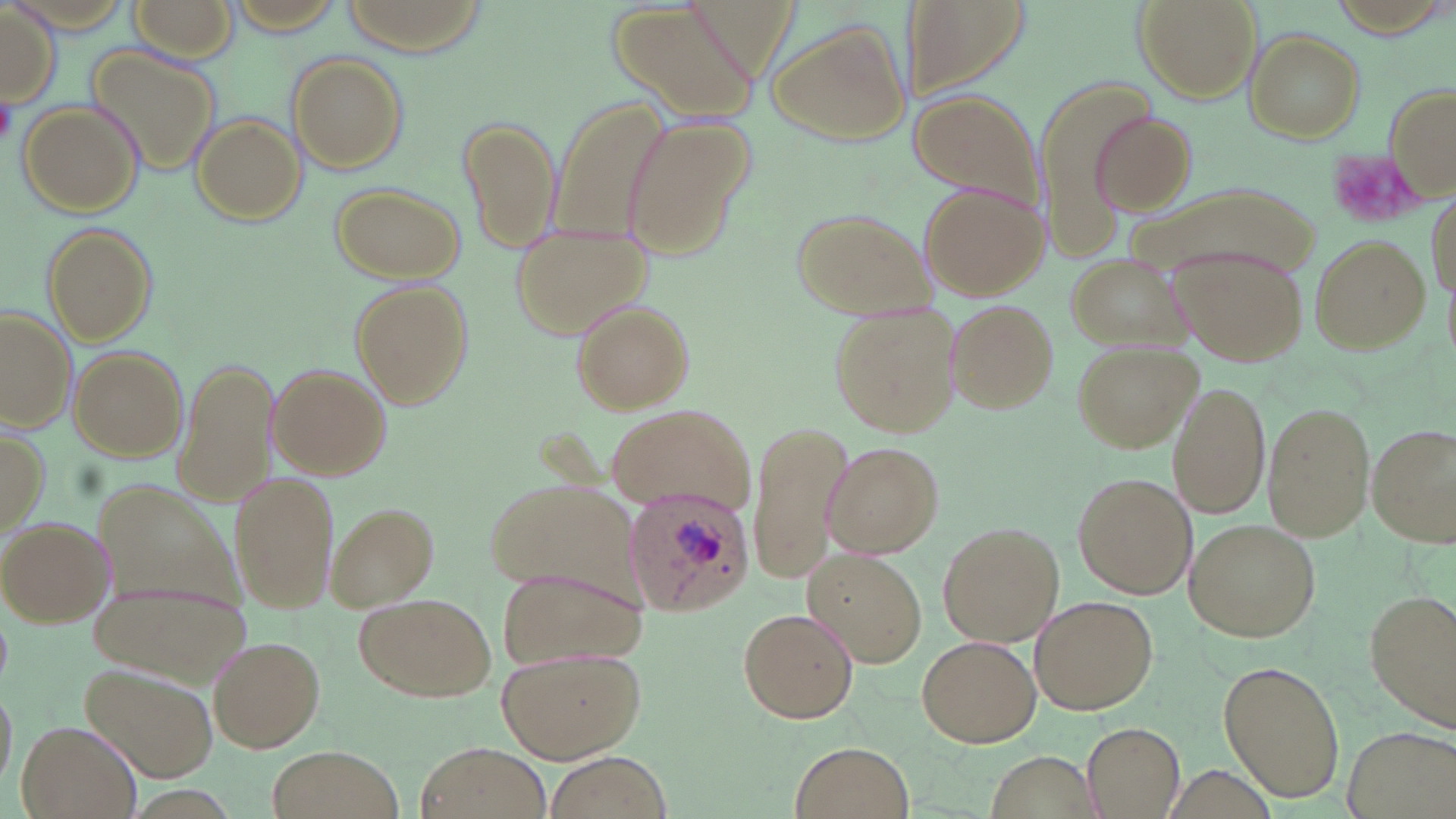

slide-level diagnosis = Plasmodium ovale
image size = 1456×819 pixels
uninfected red blood cell locations = approximate bounding boxes as named x1/y1/x2/y2 corners in pixels: (x1=133, y1=0, x2=240, y2=59), (x1=336, y1=0, x2=490, y2=52), (x1=898, y1=0, x2=1028, y2=104), (x1=1133, y1=0, x2=1259, y2=103), (x1=1330, y1=0, x2=1446, y2=37), (x1=604, y1=2, x2=757, y2=127), (x1=1, y1=7, x2=58, y2=105), (x1=765, y1=20, x2=911, y2=146), (x1=1245, y1=31, x2=1365, y2=142), (x1=86, y1=44, x2=222, y2=178), (x1=285, y1=50, x2=408, y2=173), (x1=1035, y1=78, x2=1143, y2=263), (x1=1384, y1=83, x2=1456, y2=201), (x1=908, y1=91, x2=1044, y2=210), (x1=549, y1=96, x2=668, y2=250), (x1=18, y1=102, x2=142, y2=219), (x1=458, y1=113, x2=561, y2=254), (x1=1092, y1=113, x2=1198, y2=213), (x1=191, y1=114, x2=306, y2=223), (x1=617, y1=120, x2=747, y2=259), (x1=1120, y1=182, x2=1326, y2=279), (x1=919, y1=183, x2=1046, y2=299), (x1=330, y1=184, x2=465, y2=282), (x1=789, y1=207, x2=934, y2=319), (x1=507, y1=223, x2=654, y2=338), (x1=40, y1=224, x2=155, y2=346), (x1=1309, y1=234, x2=1430, y2=353), (x1=1172, y1=246, x2=1308, y2=366), (x1=1065, y1=252, x2=1189, y2=349), (x1=350, y1=280, x2=471, y2=408), (x1=945, y1=299, x2=1057, y2=414), (x1=571, y1=300, x2=694, y2=415), (x1=829, y1=300, x2=960, y2=438), (x1=1, y1=308, x2=76, y2=433), (x1=1071, y1=341, x2=1200, y2=454), (x1=68, y1=345, x2=188, y2=462), (x1=176, y1=354, x2=278, y2=508), (x1=268, y1=365, x2=392, y2=479), (x1=1170, y1=383, x2=1270, y2=520), (x1=1263, y1=401, x2=1375, y2=543), (x1=606, y1=402, x2=756, y2=519), (x1=748, y1=419, x2=854, y2=588), (x1=1366, y1=422, x2=1456, y2=548), (x1=1, y1=426, x2=46, y2=534), (x1=823, y1=441, x2=943, y2=559), (x1=228, y1=468, x2=338, y2=613), (x1=1075, y1=472, x2=1198, y2=600), (x1=488, y1=478, x2=636, y2=593), (x1=328, y1=502, x2=440, y2=612), (x1=0, y1=515, x2=110, y2=627), (x1=1185, y1=518, x2=1320, y2=642), (x1=937, y1=522, x2=1063, y2=645), (x1=804, y1=550, x2=928, y2=668), (x1=495, y1=568, x2=644, y2=668), (x1=91, y1=575, x2=248, y2=686), (x1=1369, y1=589, x2=1456, y2=727), (x1=355, y1=590, x2=498, y2=701), (x1=1031, y1=595, x2=1158, y2=716), (x1=735, y1=606, x2=860, y2=724), (x1=917, y1=634, x2=1039, y2=747), (x1=208, y1=635, x2=326, y2=754), (x1=497, y1=644, x2=645, y2=762), (x1=1218, y1=659, x2=1345, y2=802), (x1=83, y1=666, x2=218, y2=782), (x1=0, y1=683, x2=16, y2=787), (x1=1081, y1=718, x2=1187, y2=819), (x1=15, y1=721, x2=141, y2=819), (x1=789, y1=740, x2=912, y2=817), (x1=416, y1=742, x2=547, y2=818), (x1=268, y1=746, x2=404, y2=819), (x1=544, y1=753, x2=672, y2=819)
modality = light microscopy
preparation = thin blood film
stain = May-Grünwald-Giemsa
field of view = single
magnification = 1000x
Plasmodium ovale-infected red blood cell locations = approximate bounding boxes as named x1/y1/x2/y2 corners in pixels: (x1=620, y1=483, x2=755, y2=614)
platelet locations = approximate bounding boxes as named x1/y1/x2/y2 corners in pixels: (x1=0, y1=91, x2=17, y2=144), (x1=1330, y1=151, x2=1432, y2=223)